Assess the morphology of the erythrocytes.
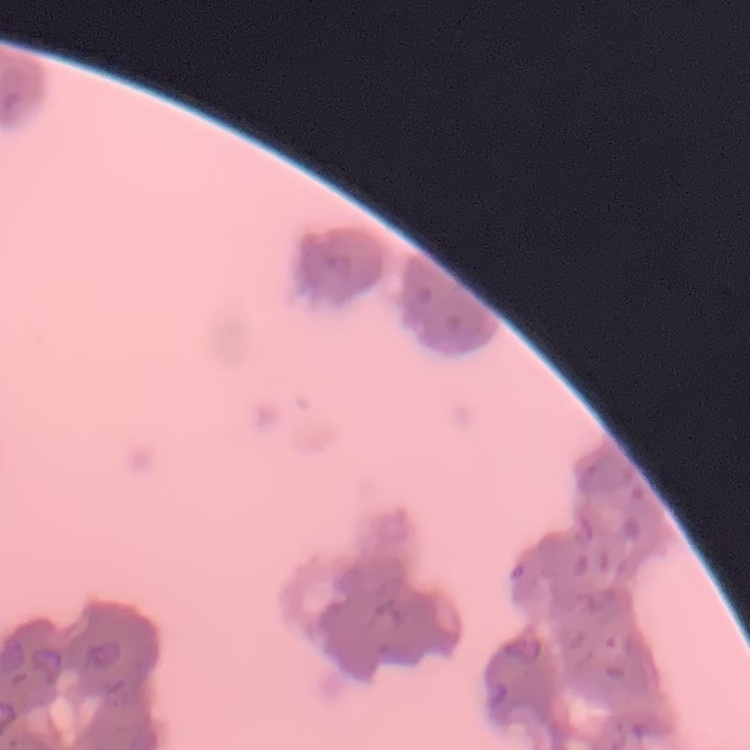

They show rouleaux formation.

image type = square crop of a larger photomicrograph
preparation = thin blood smear
stain = Field's or Giemsa